Give the position of every malaria parasite and every leukocyte.
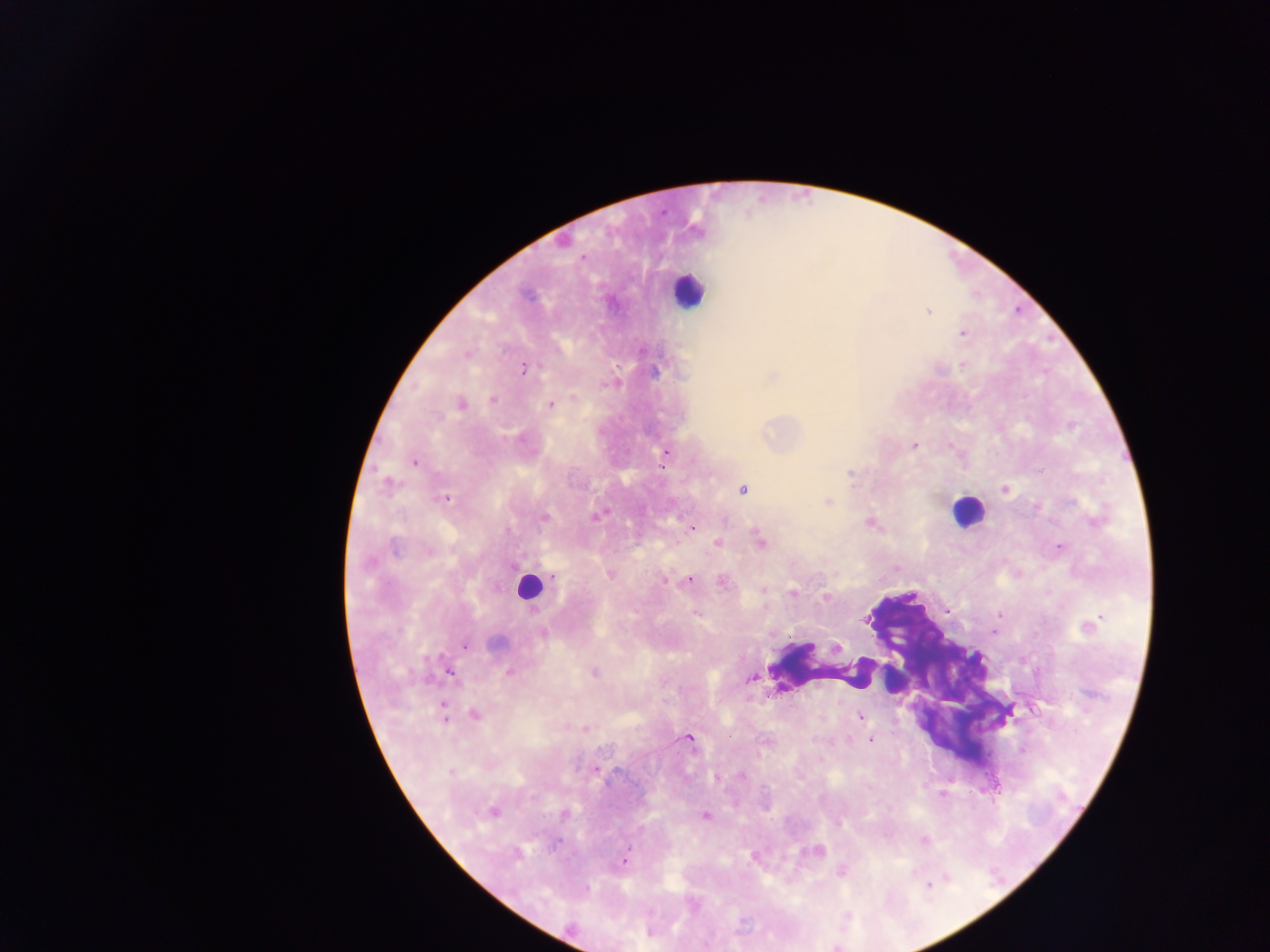
Approximate centers as [x, y] in pixels.
Malaria parasites: [583, 256], [928, 311], [962, 333], [467, 355], [523, 368], [655, 372], [773, 376], [575, 397], [492, 400], [461, 404], [550, 405], [914, 446], [665, 452], [414, 462], [851, 474], [386, 483], [1005, 489], [743, 490], [444, 499], [828, 500], [1036, 507], [597, 515], [544, 517], [1096, 521], [869, 522], [690, 528], [759, 540], [718, 542], [1060, 547], [394, 549], [610, 574], [554, 576], [689, 579], [665, 580], [722, 582], [793, 593], [825, 597], [696, 614], [1088, 626], [543, 634], [495, 643], [466, 646], [837, 648], [449, 671], [594, 672], [509, 673], [752, 679], [443, 709], [474, 715], [860, 717], [585, 729], [689, 738], [870, 740], [451, 771], [742, 775], [716, 777], [493, 811], [565, 815], [706, 816], [838, 824], [924, 840], [818, 850], [517, 853], [626, 857], [842, 871], [929, 885], [585, 889].
Leukocytes: [687, 291], [966, 511], [528, 587], [824, 665], [891, 680].

country = Ghana
preparation = thick blood film
image size = 1270×952 pixels
field of view = single
capture = mobile-phone photograph through a microscope